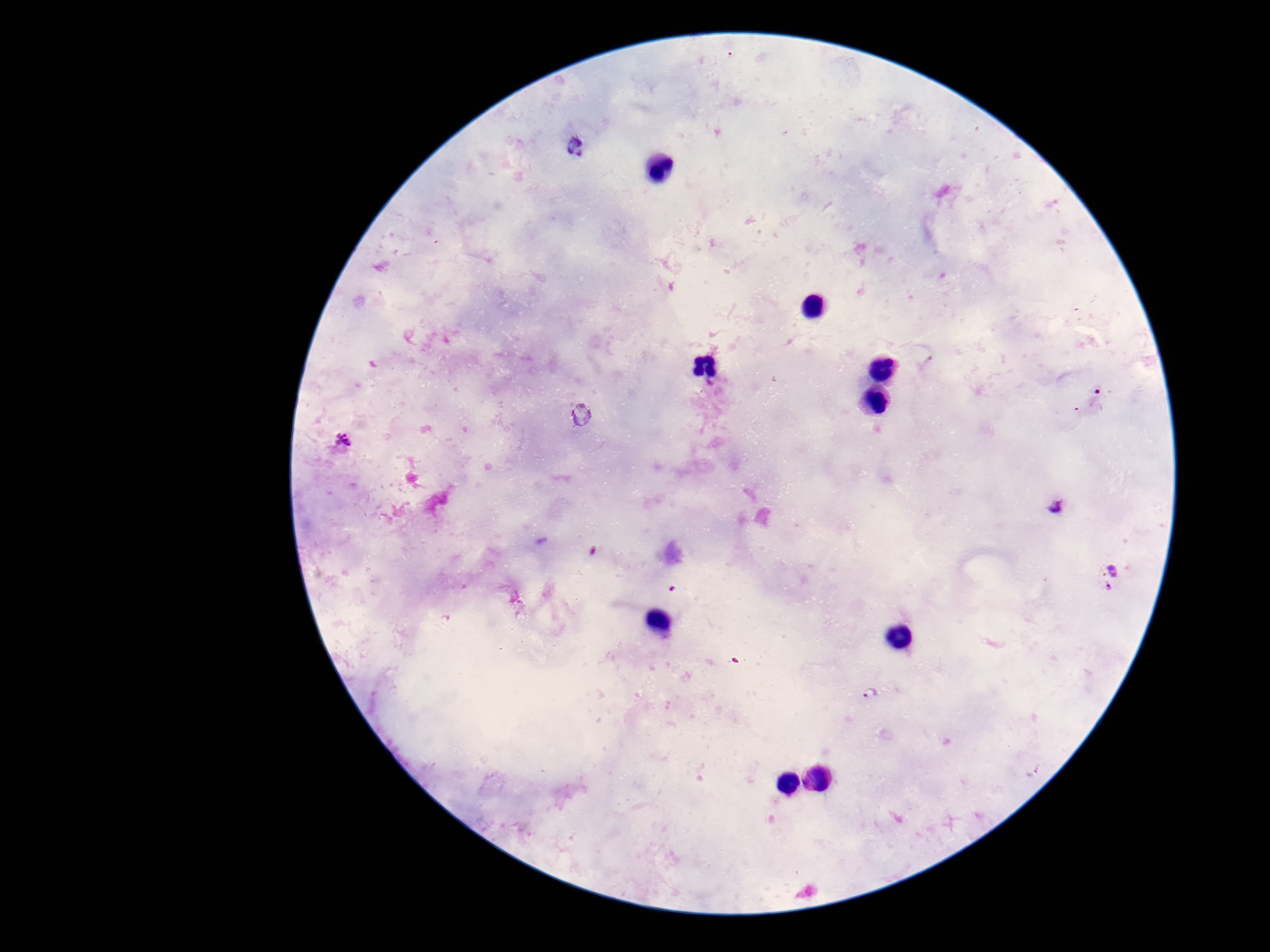

patient malaria status = positive
image size = 1270×952 pixels
stain = Giemsa
preparation = thick blood smear
field of view = one from this slide
capture = smartphone camera through the microscope eyepiece
magnification = 100x
Plasmodium parasite locations = approximate object centers, in pixels from the top-left corner: (x=577, y=146), (x=1097, y=396), (x=581, y=413), (x=347, y=443), (x=1054, y=509), (x=1110, y=577), (x=872, y=694)